Assess this cell for malaria.
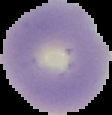
Uninfected.

image size = 112×115 pixels
image type = segmented cell region with the area outside set to black
preparation = thin blood smear